Give the position of every Plasmodium parasite visible.
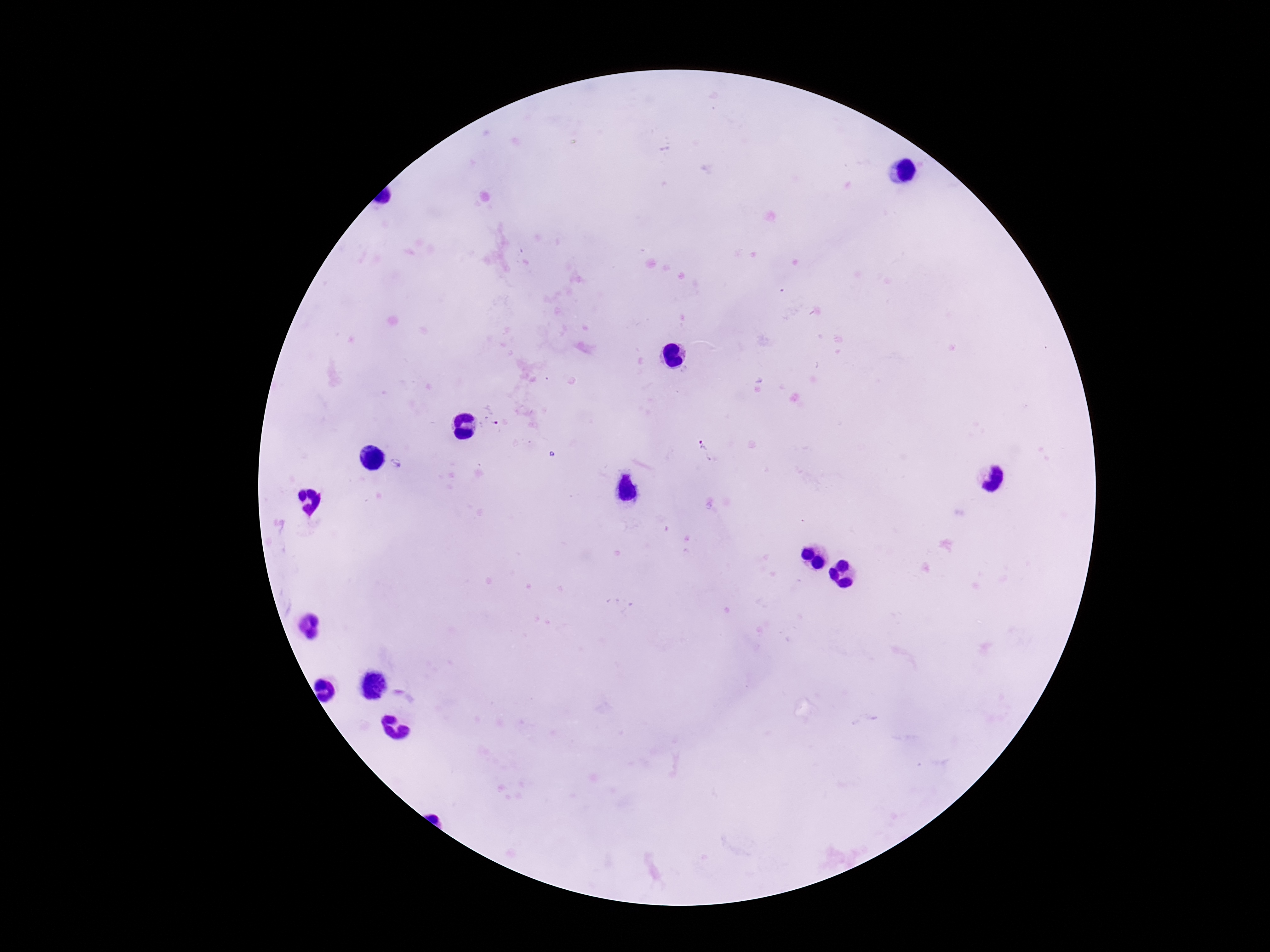

Approximate centers as [x, y] in pixels.
Plasmodium parasites: [489, 423], [707, 454].

Thick peripheral-blood smear. Patient malaria status: infected. Single field of view. 100x magnification. Image is 1270×952 pixels. Giemsa stain. Photographed through the microscope eyepiece with a smartphone camera.